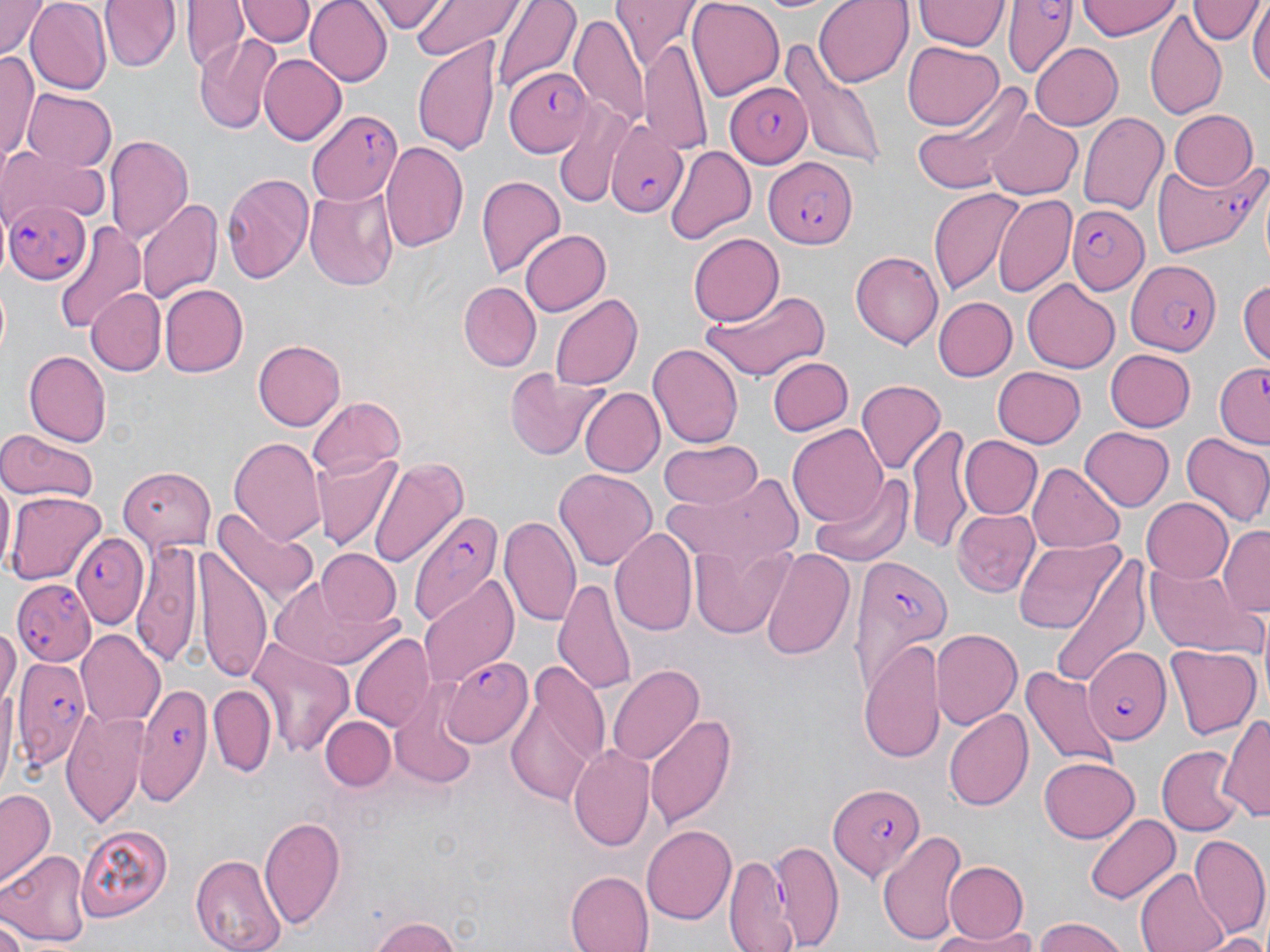
Summary:
  - Coordinate format: approximate bounding boxes as (x1,y1)-(x2,y2) corner pairs in pixels
  - Plasmodium falciparum-infected red blood cell locations: (1004,0)-(1074,80), (502,66)-(592,154), (724,81)-(812,166), (306,108)-(404,207), (605,120)-(687,218), (765,157)-(857,250), (1153,157)-(1265,256), (2,195)-(91,285), (1065,201)-(1150,298), (1126,258)-(1225,357), (1213,363)-(1270,451), (406,511)-(500,627), (70,531)-(149,628), (848,553)-(955,691), (12,579)-(97,666), (1085,648)-(1170,742), (12,656)-(92,765), (442,659)-(531,749), (125,681)-(212,810), (829,783)-(924,882)
  - Uninfected red blood cell locations: (0,0)-(50,57), (25,0)-(112,93), (100,0)-(180,71), (183,0)-(248,74), (304,0)-(391,86), (372,0)-(444,34), (411,0)-(521,60), (491,0)-(582,93), (687,0)-(784,99), (814,0)-(913,87), (914,0)-(1006,53), (1079,0)-(1181,40), (1194,0)-(1259,47), (1250,0)-(1269,94), (237,1)-(314,49), (615,2)-(701,74), (1145,8)-(1227,119), (571,13)-(651,130), (195,35)-(279,134), (413,36)-(502,156), (780,38)-(885,169), (639,39)-(713,153), (902,42)-(1004,131), (1029,42)-(1124,130), (1,54)-(39,167), (259,54)-(346,146), (23,87)-(117,170), (915,88)-(1030,196), (550,100)-(638,211), (985,108)-(1083,201), (1167,110)-(1259,190), (1078,112)-(1169,215), (105,136)-(194,244), (380,140)-(469,254), (665,145)-(755,242), (0,147)-(109,226), (222,173)-(316,285), (477,175)-(566,277), (304,184)-(398,290), (927,187)-(1025,297), (994,193)-(1076,297), (137,197)-(222,306), (52,222)-(147,338), (518,229)-(611,316), (688,233)-(783,326), (850,250)-(943,350), (1238,278)-(1270,368), (1022,279)-(1120,372), (459,281)-(541,372), (159,285)-(246,378), (89,288)-(165,374), (701,288)-(832,383), (550,293)-(641,392), (933,296)-(1017,381), (253,341)-(345,429), (647,342)-(743,449), (1104,349)-(1196,432), (25,351)-(112,445), (768,356)-(853,436), (992,365)-(1087,447), (503,369)-(607,460), (856,379)-(944,474), (580,387)-(664,477), (309,395)-(403,481), (788,424)-(889,528), (908,426)-(977,552), (1081,427)-(1176,512), (1179,429)-(1270,527), (0,432)-(99,502), (962,436)-(1041,519), (230,437)-(327,547), (658,440)-(761,510), (314,453)-(403,550), (370,457)-(467,566), (117,462)-(216,550), (1029,462)-(1123,552), (553,467)-(658,573), (808,472)-(914,569), (665,473)-(802,571), (1,477)-(15,573), (7,491)-(105,585), (1143,498)-(1234,581), (214,504)-(318,608), (952,510)-(1039,597), (501,514)-(583,631), (1219,525)-(1270,615), (613,527)-(697,638), (1012,537)-(1124,637), (134,539)-(202,669), (200,540)-(271,686), (688,541)-(793,639), (759,546)-(853,662), (315,550)-(400,628), (1051,553)-(1152,691), (1149,561)-(1253,652), (419,575)-(518,688), (552,576)-(636,696), (269,578)-(395,671), (0,622)-(20,704), (931,628)-(1022,731), (77,631)-(165,727), (350,632)-(434,731), (248,638)-(354,755), (860,640)-(943,762), (1166,644)-(1260,741), (505,658)-(609,807), (606,663)-(705,766), (1018,665)-(1119,772), (0,678)-(18,797), (208,683)-(277,776), (391,690)-(479,789), (945,707)-(1034,812), (63,708)-(150,829), (1220,711)-(1270,825), (646,713)-(737,830), (322,715)-(394,792), (568,743)-(657,853), (1154,745)-(1241,836), (1040,756)-(1139,841), (1,789)-(56,884), (1085,812)-(1181,905), (260,815)-(347,930), (75,822)-(175,921), (642,823)-(736,922), (877,830)-(970,945), (1189,835)-(1270,938), (774,840)-(843,950), (1,851)-(91,948), (722,851)-(796,952), (192,852)-(288,951), (945,861)-(1027,942), (1136,869)-(1229,952), (566,871)-(654,952), (366,915)-(465,952), (1032,916)-(1132,952), (0,918)-(26,952), (924,929)-(1035,950), (1207,932)-(1270,952)
  - Slide-level diagnosis: Plasmodium falciparum
  - Image size: 1270×952 pixels
  - Field of view: one of a larger specimen
  - Magnification: 1000x
  - Modality: light microscopy
  - Stain: May-Grünwald-Giemsa
  - Preparation: thin blood smear